State the blood parasite species.
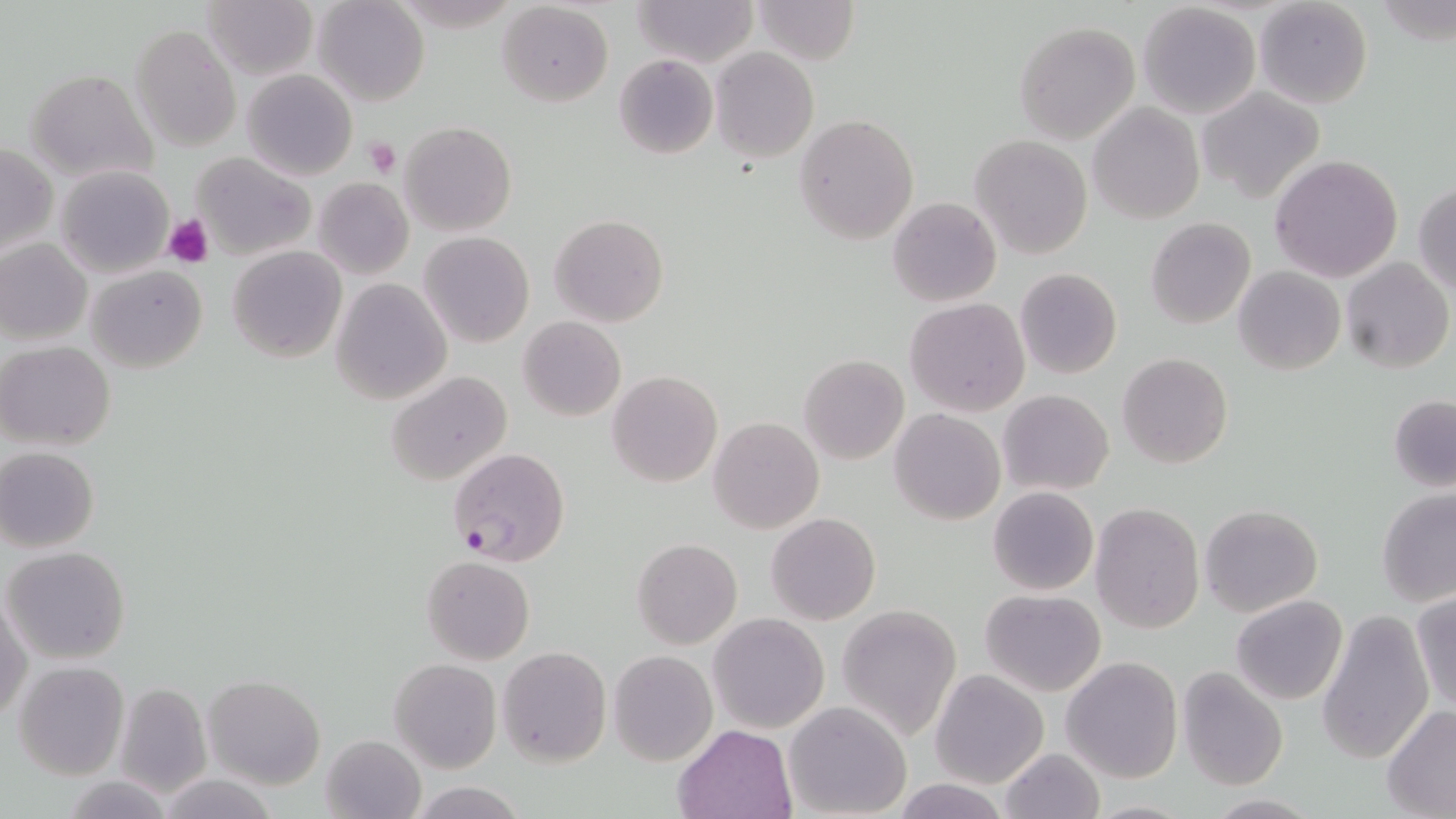

Plasmodium falciparum.

Approximate bounding boxes as (x1, y1, x2, y2) in pixels. Uninfected red blood cell locations: (201, 0, 318, 81), (313, 0, 428, 107), (633, 0, 759, 67), (751, 0, 860, 65), (1254, 0, 1373, 110), (497, 1, 613, 109), (1137, 3, 1261, 118), (1014, 21, 1140, 143), (132, 23, 241, 152), (711, 47, 819, 163), (614, 53, 719, 157), (242, 68, 357, 180), (27, 69, 158, 185), (1199, 86, 1324, 202), (1088, 102, 1204, 224), (795, 114, 920, 246), (399, 121, 517, 237), (970, 135, 1092, 258), (1, 144, 55, 256), (190, 152, 316, 260), (1269, 154, 1404, 283), (55, 165, 174, 277), (316, 178, 415, 279), (1413, 182, 1456, 294), (887, 196, 1001, 307), (549, 214, 669, 326), (1146, 217, 1256, 330), (418, 232, 534, 349), (0, 240, 91, 345), (227, 246, 347, 363), (1340, 257, 1452, 373), (86, 265, 208, 372), (1232, 266, 1345, 375), (1015, 267, 1122, 379), (331, 278, 451, 405), (905, 298, 1030, 417), (518, 316, 625, 422), (1, 341, 117, 451), (1117, 353, 1233, 470), (798, 355, 909, 464), (386, 371, 511, 487), (607, 371, 722, 489), (997, 389, 1114, 495), (1389, 396, 1456, 491), (889, 409, 1005, 525), (708, 418, 824, 535), (0, 447, 100, 552), (988, 486, 1098, 596), (1377, 487, 1456, 606), (1091, 501, 1206, 633), (1199, 503, 1323, 617), (766, 513, 880, 626), (632, 538, 742, 649), (4, 545, 132, 663), (422, 554, 534, 664), (980, 589, 1106, 695), (1, 590, 31, 724), (1410, 591, 1456, 714), (1231, 594, 1347, 705), (836, 604, 961, 742), (1318, 610, 1434, 765), (708, 613, 829, 734), (497, 646, 611, 767), (609, 650, 716, 765), (1062, 657, 1182, 784), (390, 658, 501, 772), (12, 661, 130, 780), (1176, 666, 1288, 790), (931, 669, 1049, 788), (204, 674, 325, 788), (114, 681, 212, 798), (783, 700, 912, 818), (1381, 704, 1455, 817), (673, 724, 798, 818), (320, 735, 428, 819), (997, 747, 1105, 819), (156, 775, 282, 819), (64, 776, 176, 817), (894, 779, 1008, 817), (409, 781, 528, 819), (1203, 795, 1325, 818). Plasmodium falciparum-infected red blood cell locations: (447, 446, 570, 568). Platelet locations: (363, 137, 402, 178), (164, 213, 215, 266). Optical microscopy. May-Grünwald-Giemsa stain. 1000x magnification. Image is 1456×819 pixels. Thin blood film. Single field of view.